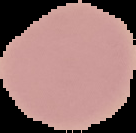

Summary:
  - Result: no malaria parasites seen
  - Image size: 136×133 pixels
  - Preparation: thin blood film
  - Image type: segmented cell region with the area outside set to black